Locate every blood parasite and identify its species.
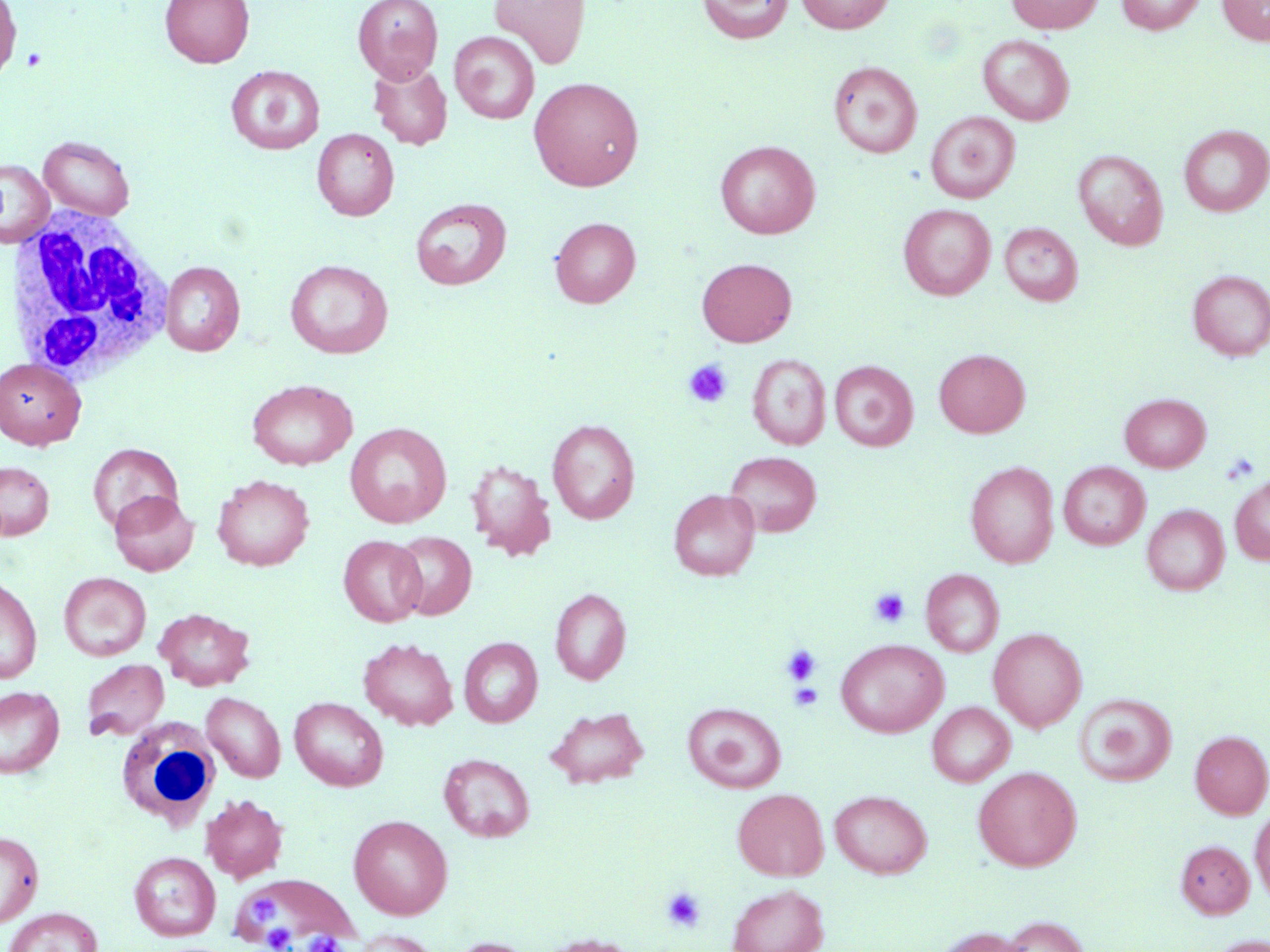

No blood parasites observed.

Summary:
  - Coordinate format: approximate bounding boxes as (x1, y1, x2, y2) in pixels
  - Uninfected red blood cell locations: (160, 0, 254, 67), (352, 0, 443, 83), (490, 0, 591, 69), (697, 0, 793, 44), (796, 0, 895, 34), (1006, 0, 1105, 34), (1117, 0, 1205, 35), (1218, 0, 1270, 46), (0, 1, 22, 86), (450, 32, 540, 123), (978, 34, 1074, 125), (828, 60, 923, 158), (369, 61, 452, 149), (226, 65, 324, 154), (528, 76, 644, 191), (926, 111, 1020, 203), (1179, 125, 1270, 216), (312, 128, 399, 221), (38, 136, 135, 220), (715, 140, 820, 239), (1073, 149, 1168, 250), (0, 158, 54, 248), (410, 198, 511, 290), (898, 204, 995, 300), (550, 217, 640, 307), (999, 222, 1083, 306), (696, 258, 797, 346), (285, 259, 393, 358), (160, 261, 245, 356), (1187, 270, 1270, 360), (933, 349, 1030, 437), (748, 354, 831, 450), (0, 358, 86, 449), (830, 360, 917, 451), (247, 379, 357, 470), (1119, 393, 1210, 472), (547, 419, 640, 524), (345, 422, 451, 528), (88, 443, 183, 533), (724, 451, 822, 536), (466, 459, 557, 561), (0, 461, 54, 540), (965, 461, 1059, 568), (1058, 462, 1150, 549), (212, 474, 314, 571), (1230, 474, 1270, 565), (669, 489, 760, 581), (109, 490, 198, 576), (1142, 504, 1230, 595), (390, 531, 476, 620), (339, 535, 426, 626), (921, 568, 1004, 657), (59, 572, 151, 661), (0, 576, 42, 684), (550, 588, 631, 684), (154, 608, 255, 690), (988, 627, 1087, 732), (459, 637, 542, 726), (358, 638, 459, 730), (835, 638, 948, 737), (81, 659, 169, 741), (0, 685, 65, 779), (202, 691, 286, 782), (1074, 693, 1177, 786), (289, 697, 388, 791), (683, 702, 786, 791), (927, 702, 1015, 786), (544, 705, 650, 789), (1190, 730, 1270, 818), (438, 753, 535, 842), (972, 766, 1081, 871), (732, 788, 828, 880), (829, 790, 932, 878), (200, 794, 288, 883), (1250, 806, 1270, 903), (349, 814, 453, 919), (0, 830, 44, 927), (1176, 839, 1255, 918), (129, 851, 220, 940), (236, 874, 357, 945), (727, 882, 829, 952), (3, 907, 104, 952), (996, 915, 1092, 952), (933, 926, 1035, 952), (349, 929, 442, 952), (535, 933, 641, 952), (1204, 934, 1269, 952), (444, 937, 538, 952)
  - White blood cell locations: (4, 206, 174, 383), (112, 720, 221, 827)
  - Platelet locations: (23, 48, 49, 71), (682, 358, 733, 408), (1221, 452, 1260, 485), (869, 588, 910, 628), (782, 644, 821, 684), (789, 683, 823, 711), (660, 886, 707, 932), (249, 896, 278, 921), (262, 924, 295, 950), (308, 932, 343, 952)
  - Slide-level diagnosis: negative for blood parasites
  - Modality: optical microscopy
  - Magnification: 1000x
  - Preparation: thin blood smear
  - Field of view: single
  - Image size: 1270×952 pixels
  - Stain: May-Grünwald-Giemsa